Comment on the morphology of the red blood cells.
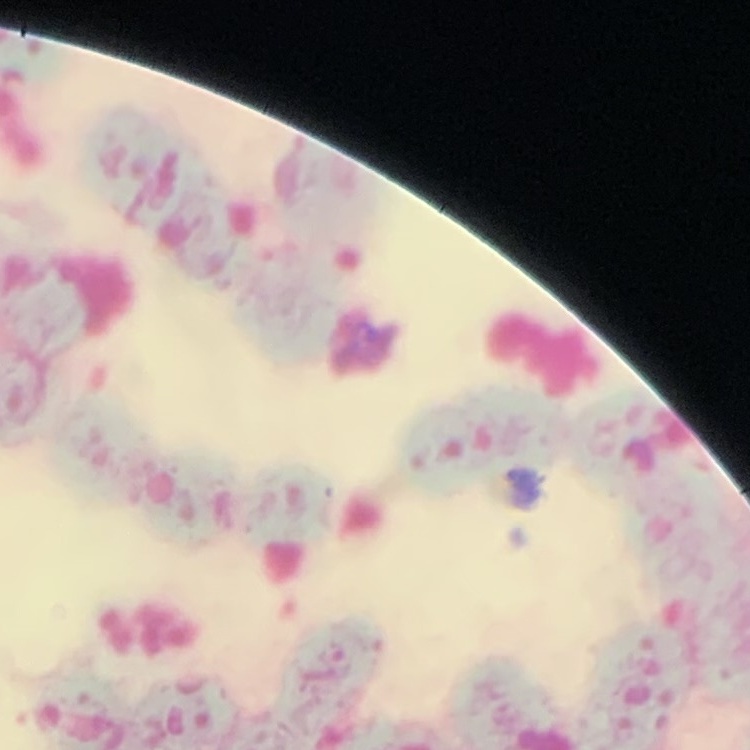
Rouleaux formation.

Summary:
  - Preparation: thin peripheral smear
  - Stain: Field's or Giemsa
  - Image type: square crop of a larger photomicrograph